Assess this cell for malaria.
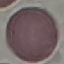
It is uninfected.

Summary:
  - Capture: smartphone through the microscope eyepiece
  - Preparation: thin blood film
  - Image type: cell patch, automatically extracted from a larger field of view and resized to 64 × 64 pixels
  - Stain: Giemsa